Give the position of every Plasmodium parasite visible.
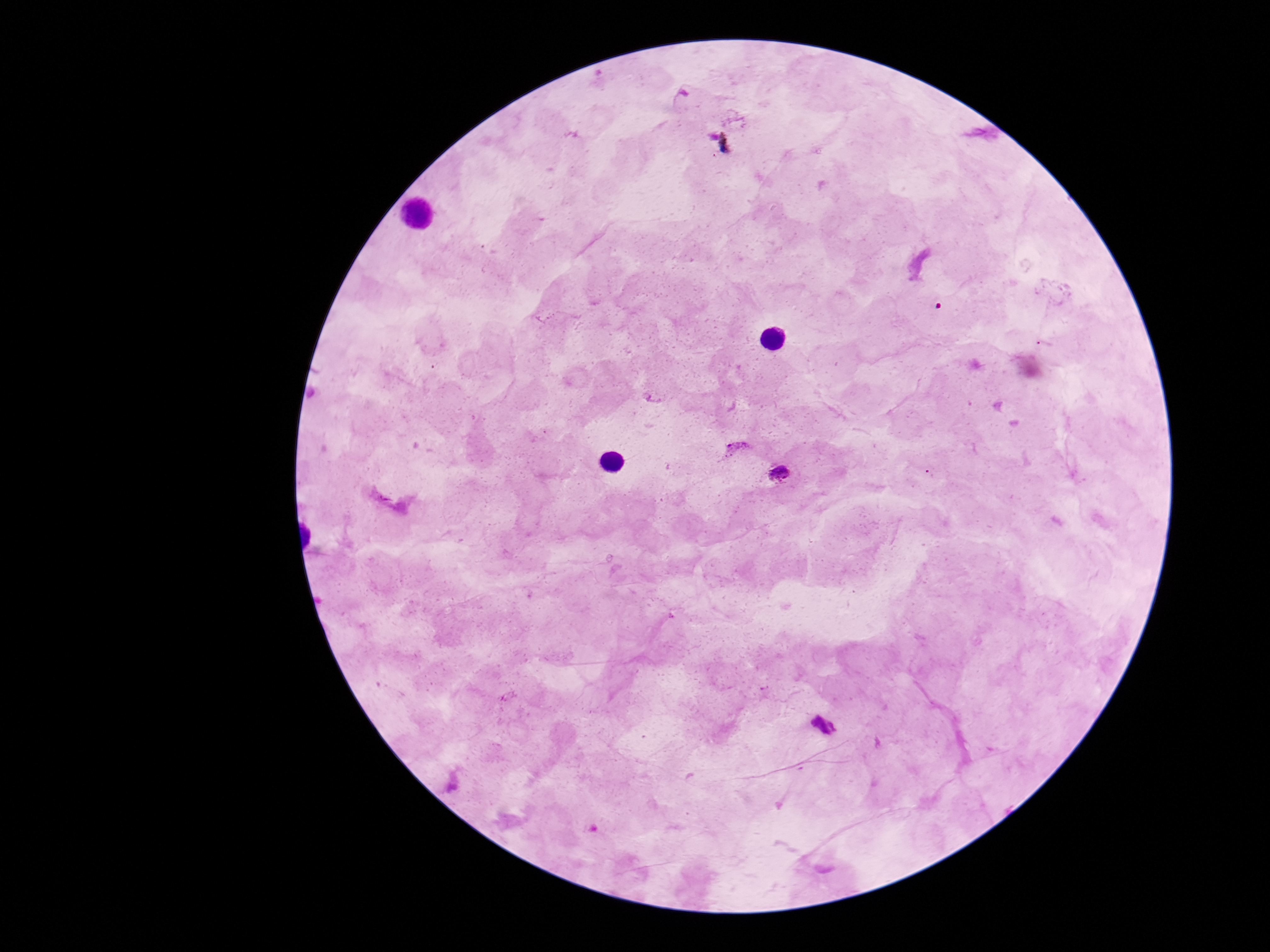
Approximate centers as [x, y] in pixels.
Plasmodium parasites: [735, 446], [780, 472], [823, 724].

Summary:
  - Field of view: one from this slide
  - Stain: Giemsa
  - Magnification: 100x
  - Image size: 1270×952 pixels
  - Preparation: thick blood smear
  - Patient malaria status: infected
  - Capture: smartphone camera through the microscope eyepiece